State which cell type is depicted.
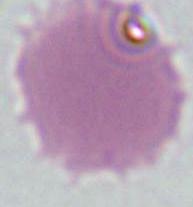
This is an erythrocyte.

modality: photomicrograph
magnification: 1000x